Assess this cell for malaria.
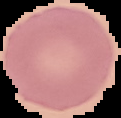
Uninfected.

{
  "preparation": "thin blood smear",
  "image_size": "121×118 pixels",
  "image_type": "segmented cell region on a black background"
}